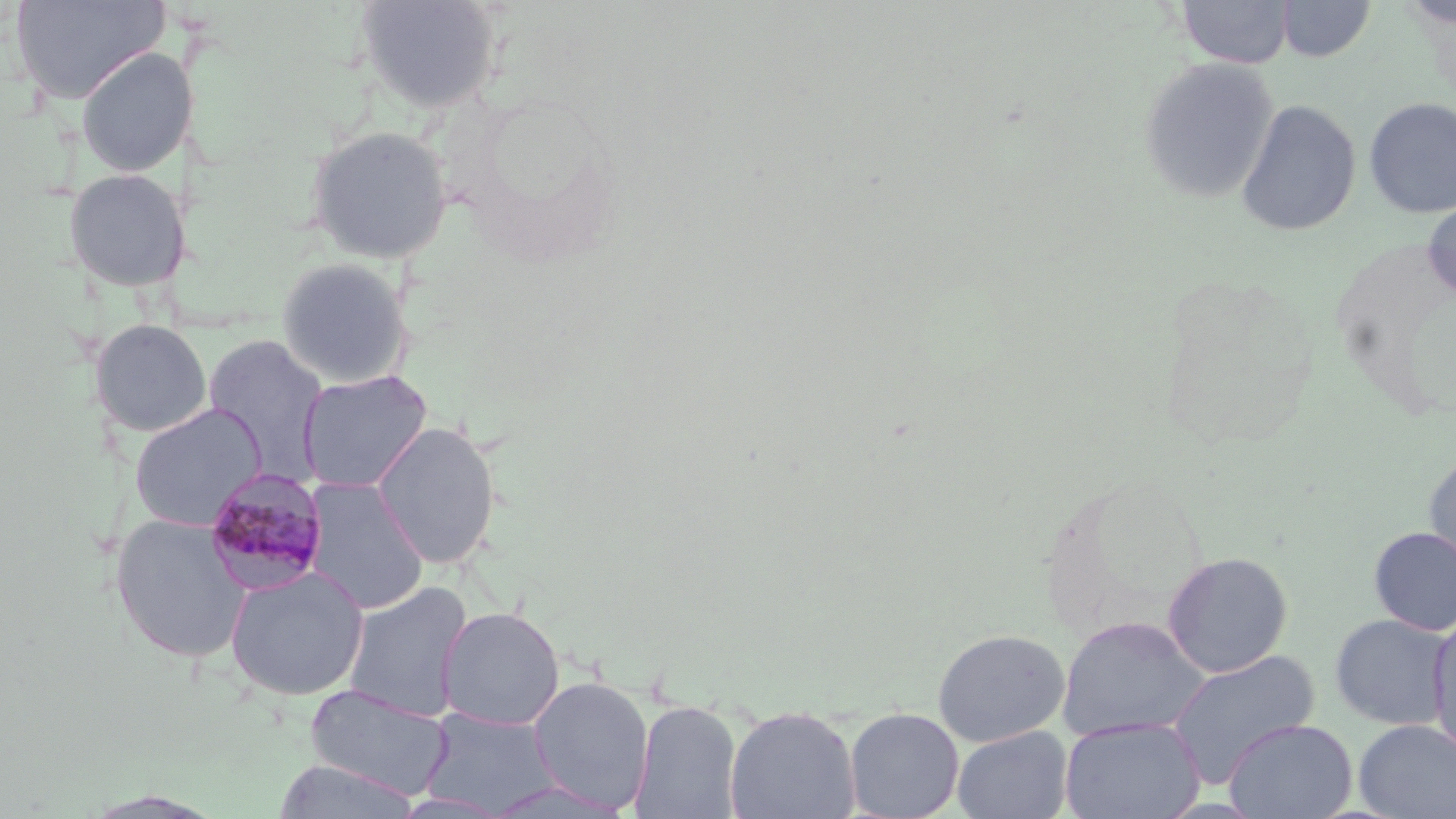

Approximate bounding boxes as named x1/y1/x2/y2 corners in pixels. Plasmodium malariae-infected red blood cell locations: (x1=202, y1=469, x2=329, y2=594). Uninfected red blood cell locations: (x1=12, y1=0, x2=168, y2=105), (x1=355, y1=0, x2=501, y2=114), (x1=1176, y1=0, x2=1294, y2=69), (x1=1276, y1=0, x2=1377, y2=63), (x1=1398, y1=1, x2=1456, y2=30), (x1=76, y1=47, x2=192, y2=178), (x1=1138, y1=57, x2=1279, y2=204), (x1=1364, y1=97, x2=1456, y2=218), (x1=1236, y1=100, x2=1361, y2=237), (x1=305, y1=125, x2=454, y2=264), (x1=63, y1=168, x2=188, y2=292), (x1=1422, y1=197, x2=1456, y2=302), (x1=275, y1=257, x2=415, y2=389), (x1=88, y1=319, x2=214, y2=438), (x1=202, y1=334, x2=330, y2=483), (x1=297, y1=369, x2=433, y2=493), (x1=128, y1=403, x2=267, y2=531), (x1=371, y1=422, x2=502, y2=569), (x1=1423, y1=447, x2=1456, y2=577), (x1=302, y1=477, x2=430, y2=614), (x1=109, y1=512, x2=253, y2=664), (x1=1369, y1=526, x2=1456, y2=635), (x1=1162, y1=551, x2=1293, y2=677), (x1=224, y1=566, x2=369, y2=701), (x1=342, y1=580, x2=474, y2=723), (x1=436, y1=606, x2=565, y2=730), (x1=1428, y1=612, x2=1456, y2=760), (x1=1329, y1=613, x2=1453, y2=729), (x1=1055, y1=615, x2=1211, y2=742), (x1=932, y1=628, x2=1070, y2=746), (x1=1165, y1=649, x2=1320, y2=787), (x1=528, y1=674, x2=655, y2=813), (x1=304, y1=683, x2=453, y2=799), (x1=629, y1=699, x2=744, y2=819), (x1=724, y1=706, x2=861, y2=819), (x1=420, y1=707, x2=561, y2=816), (x1=844, y1=708, x2=964, y2=819), (x1=1059, y1=717, x2=1206, y2=819), (x1=1223, y1=718, x2=1357, y2=819), (x1=1353, y1=719, x2=1456, y2=819), (x1=951, y1=725, x2=1074, y2=819), (x1=270, y1=758, x2=422, y2=818), (x1=484, y1=779, x2=633, y2=818). Slide-level diagnosis: Plasmodium malariae. May-Grünwald-Giemsa stain. 1000x magnification. Single field of view. Image is 1456×819 pixels. Thin blood smear. Light microscopy.